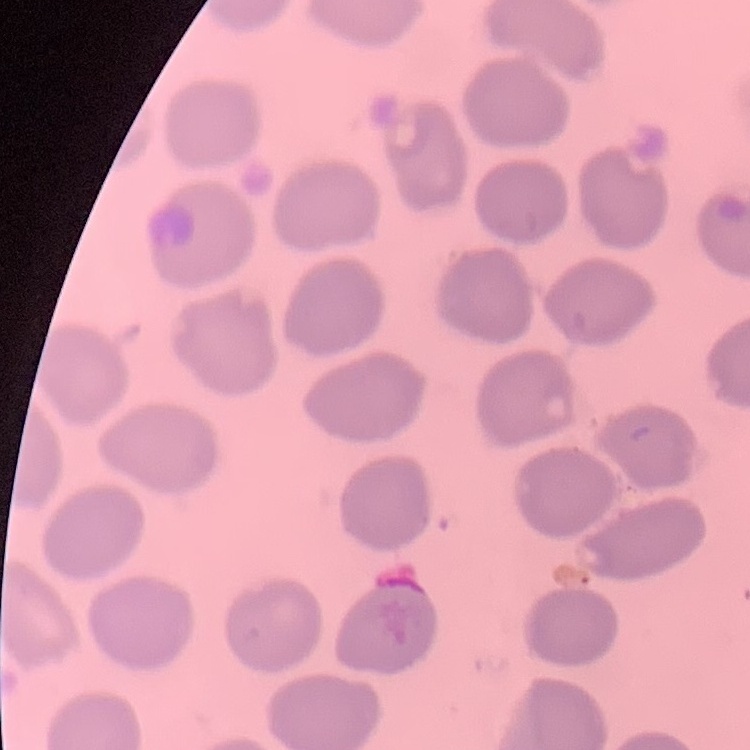

erythrocyte morphology = no rouleaux formation
image type = square crop of a larger photomicrograph
preparation = thin peripheral smear
stain = Field's or Giemsa